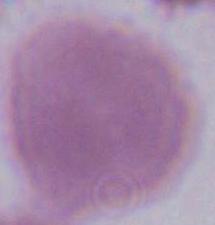
Photomicrograph. 1000x magnification. A red blood cell is seen.